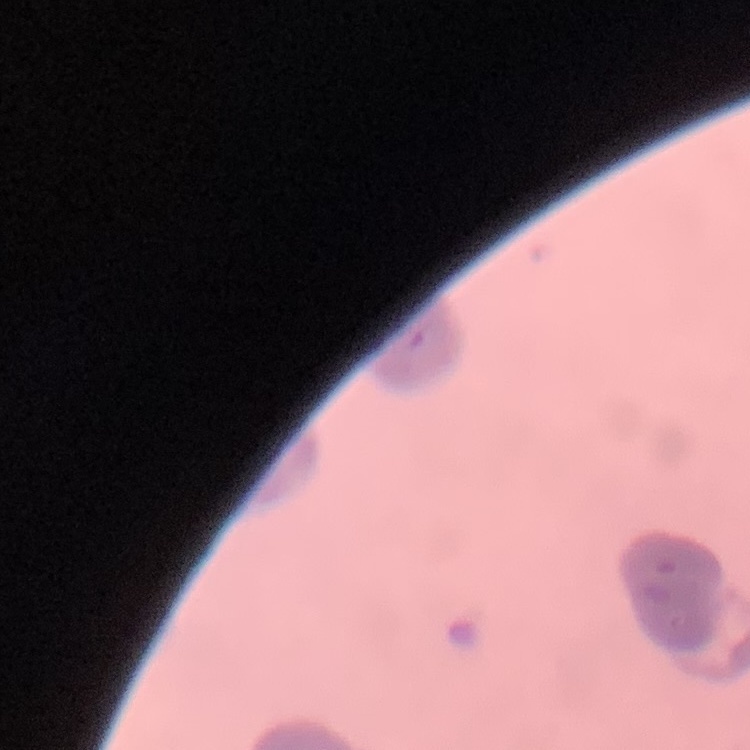
Summary:
  - Erythrocyte morphology: rouleaux formation
  - Stain: Field's or Giemsa
  - Image type: square crop of a larger photomicrograph
  - Preparation: thin peripheral smear